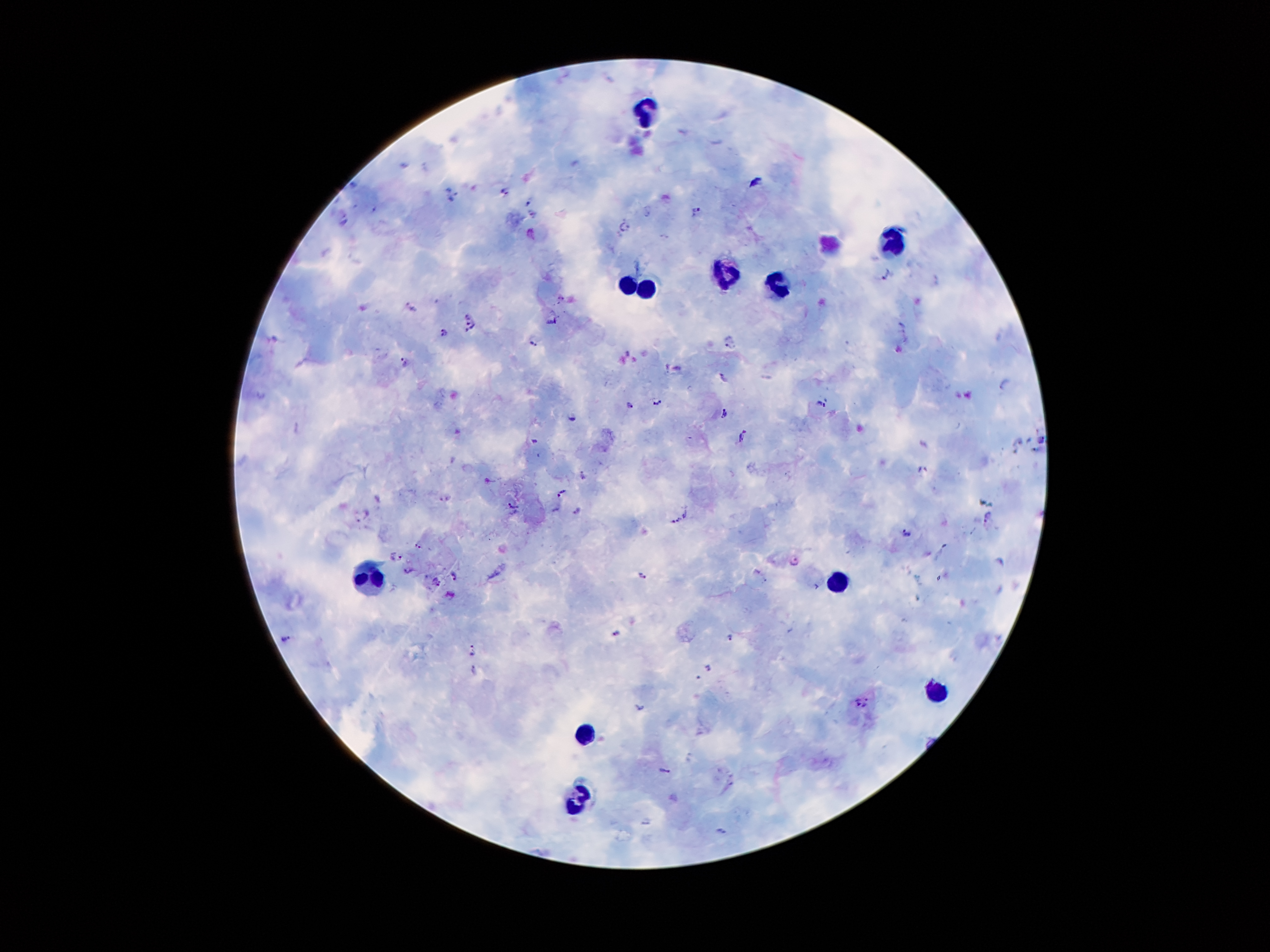
Approximate object centers, in pixels from the top-left corner. Malaria parasite locations: (x=355, y=181), (x=505, y=189), (x=527, y=201), (x=695, y=211), (x=533, y=213), (x=344, y=220), (x=625, y=224), (x=886, y=272), (x=411, y=308), (x=551, y=320), (x=473, y=323), (x=901, y=326), (x=443, y=332), (x=535, y=343), (x=729, y=344), (x=403, y=362), (x=724, y=376), (x=1004, y=384), (x=657, y=401), (x=630, y=404), (x=820, y=404), (x=723, y=411), (x=570, y=418), (x=743, y=433), (x=1041, y=436), (x=534, y=440), (x=1017, y=440), (x=924, y=444), (x=1034, y=449), (x=922, y=470), (x=583, y=477), (x=562, y=492), (x=511, y=506), (x=555, y=510), (x=578, y=511), (x=685, y=512), (x=362, y=516), (x=988, y=517), (x=675, y=520), (x=972, y=528), (x=906, y=533), (x=418, y=545), (x=395, y=556), (x=793, y=561), (x=1000, y=561), (x=409, y=570), (x=642, y=574), (x=454, y=576), (x=437, y=582), (x=618, y=634), (x=730, y=638), (x=287, y=639), (x=474, y=651), (x=710, y=667), (x=474, y=672), (x=856, y=703), (x=866, y=703), (x=641, y=708), (x=666, y=770), (x=645, y=823), (x=722, y=832). Leukocyte locations: (x=638, y=107), (x=887, y=241), (x=725, y=278), (x=625, y=282), (x=780, y=289), (x=644, y=293), (x=834, y=578), (x=368, y=582), (x=936, y=692), (x=585, y=735), (x=578, y=797). Giemsa stain. 100x magnification. Photographed through the microscope eyepiece with a smartphone camera. One field from this slide. Patient malaria status: infected with Plasmodium falciparum. Image is 1270×952 pixels. Thick blood film.